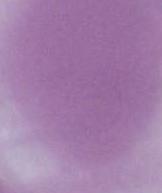

Summary:
  - Identification: red blood cell
  - Modality: micrograph
  - Magnification: 1000x